State which parasite is depicted.
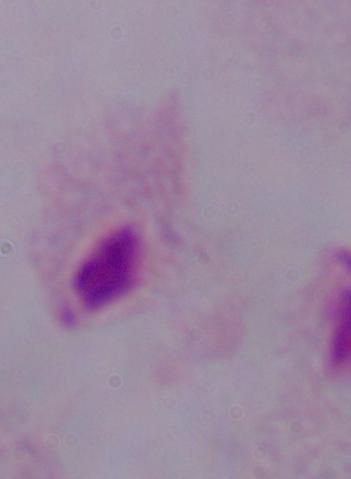
A trichomonad.

modality: photomicrograph
magnification: 1000x